Classify this cell by malaria status.
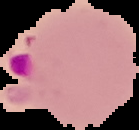

It is parasitized.

Summary:
  - Image type: segmented cell region with the area outside set to black
  - Image size: 139×130 pixels
  - Preparation: thin blood film